State which cell type is depicted.
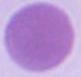

An erythrocyte.

Summary:
  - Modality: micrograph
  - Magnification: 1000x